Point out each malaria parasite and each leukocyte.
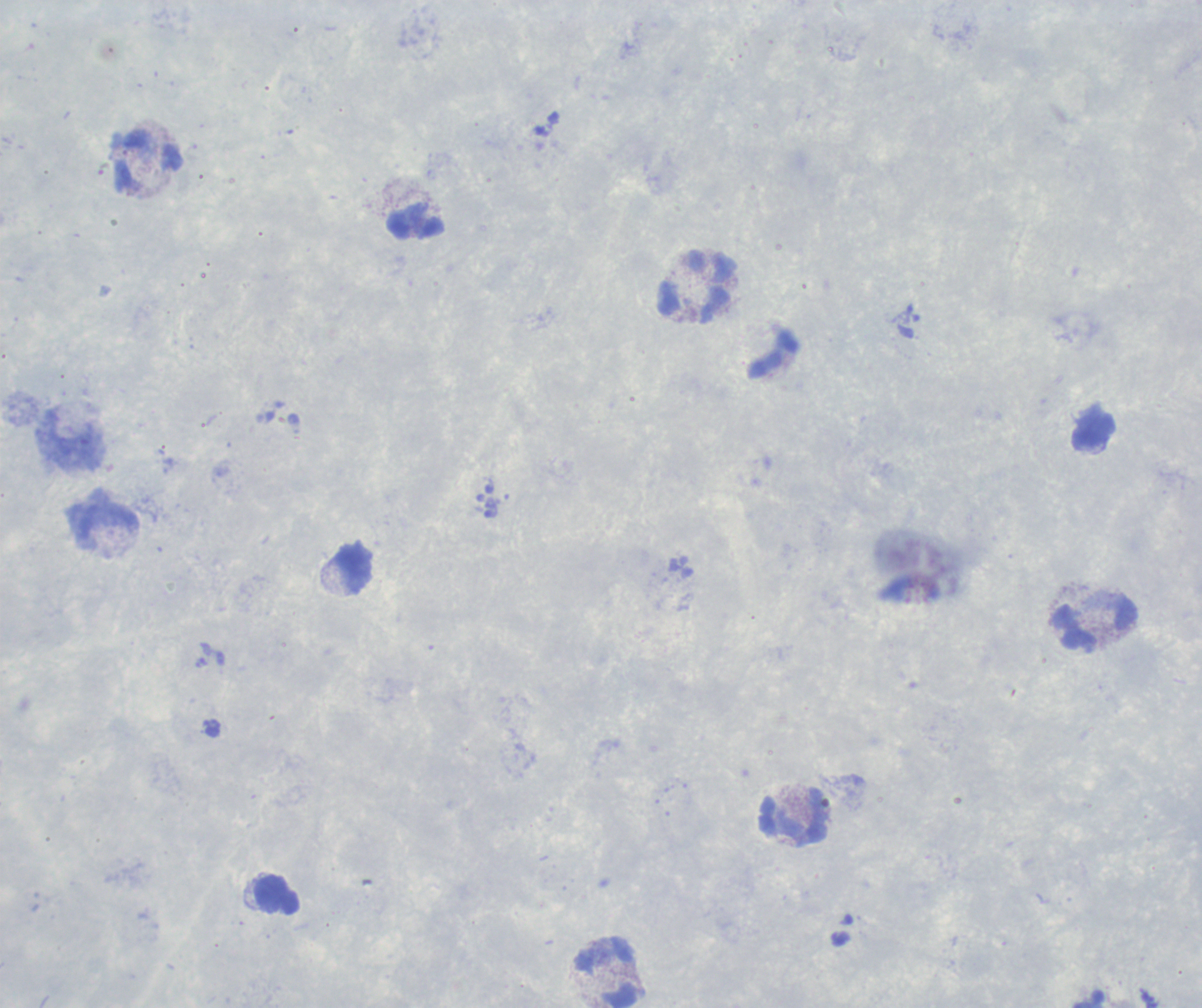
Negative for malaria parasites.
Approximate centers as [x, y] in pixels.
Leukocytes: [148, 163], [416, 222], [697, 286], [71, 443], [105, 520], [353, 567], [1097, 626], [796, 816], [277, 895], [608, 974].

Summary:
  - Stain: Romanowsky
  - Context: previously used in an actual diagnosis
  - Magnification: 100x
  - Field of view: single
  - Preparation: thick blood film
  - Coloration quality: good
  - Image size: 1202×1008 pixels
  - Background quality: poor